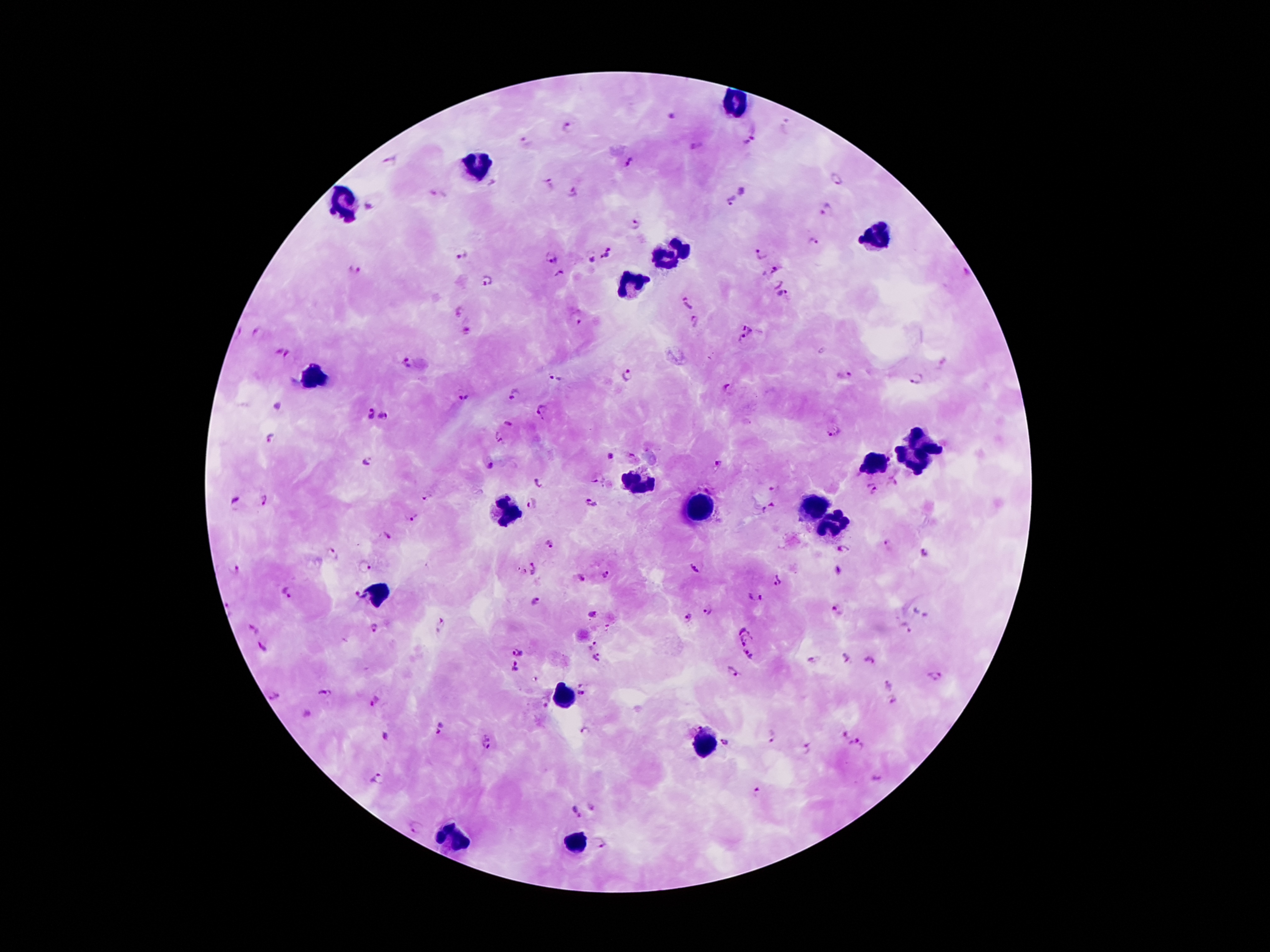
Approximate centers as [x, y] in pixels.
Summary:
  - Malaria parasite locations: [671, 116], [568, 127], [748, 142], [528, 143], [697, 148], [390, 162], [630, 163], [836, 179], [550, 183], [573, 191], [742, 192], [732, 201], [369, 206], [827, 209], [636, 224], [815, 241], [462, 251], [764, 252], [607, 254], [551, 258], [591, 258], [354, 269], [771, 271], [559, 275], [487, 279], [777, 285], [782, 295], [690, 304], [457, 310], [576, 317], [696, 320], [466, 331], [749, 331], [259, 334], [741, 339], [282, 353], [403, 363], [845, 374], [630, 376], [554, 379], [917, 379], [727, 390], [514, 394], [462, 396], [543, 411], [368, 413], [384, 415], [508, 423], [833, 432], [271, 437], [498, 439], [610, 457], [368, 462], [719, 464], [489, 465], [598, 480], [539, 484], [893, 485], [774, 486], [872, 488], [427, 497], [266, 499], [233, 501], [590, 503], [530, 504], [769, 509], [411, 516], [383, 537], [548, 544], [888, 547], [841, 551], [926, 553], [334, 555], [363, 568], [237, 569], [531, 569], [693, 570], [607, 576], [580, 579], [778, 583], [289, 592], [356, 595], [536, 598], [754, 598], [838, 609], [708, 611], [592, 613], [688, 618], [442, 624], [742, 624], [373, 628], [906, 629], [254, 630], [747, 641], [589, 645], [262, 648], [520, 650], [596, 656], [747, 657], [844, 658], [869, 660], [816, 661], [514, 669], [731, 672], [936, 677], [891, 684], [582, 687], [324, 695], [274, 696], [373, 701], [542, 701], [892, 701], [438, 728], [586, 732], [842, 733], [772, 735], [385, 737], [487, 742], [727, 743], [856, 745], [808, 748], [377, 779], [876, 783], [757, 793], [590, 805], [575, 811], [418, 830], [602, 845]
  - Leukocyte locations: [733, 104], [473, 169], [343, 205], [872, 233], [670, 254], [631, 284], [311, 375], [926, 438], [912, 459], [876, 461], [633, 484], [698, 512], [811, 512], [509, 514], [830, 527], [377, 595], [565, 697], [702, 744], [450, 842], [572, 844]
  - Patient malaria status: infected with Plasmodium falciparum
  - Image size: 1270×952 pixels
  - Stain: Giemsa
  - Capture: smartphone camera through the microscope eyepiece
  - Magnification: 100x
  - Field of view: one from this slide
  - Preparation: thick peripheral-blood smear